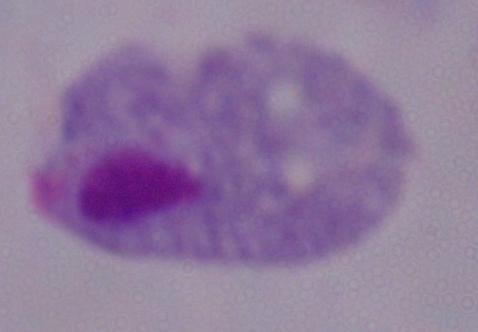

identification: trichomonad
modality: photomicrograph
magnification: 1000x